Report the malaria status of this cell.
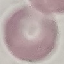
It is uninfected.

Summary:
  - Capture: smartphone camera at the microscope eyepiece
  - Stain: Giemsa
  - Preparation: thin blood smear
  - Image type: automatically extracted cell patch, resized to 64 × 64 pixels